Give the extent of all Plasmodium falciparum-infected red blood cells.
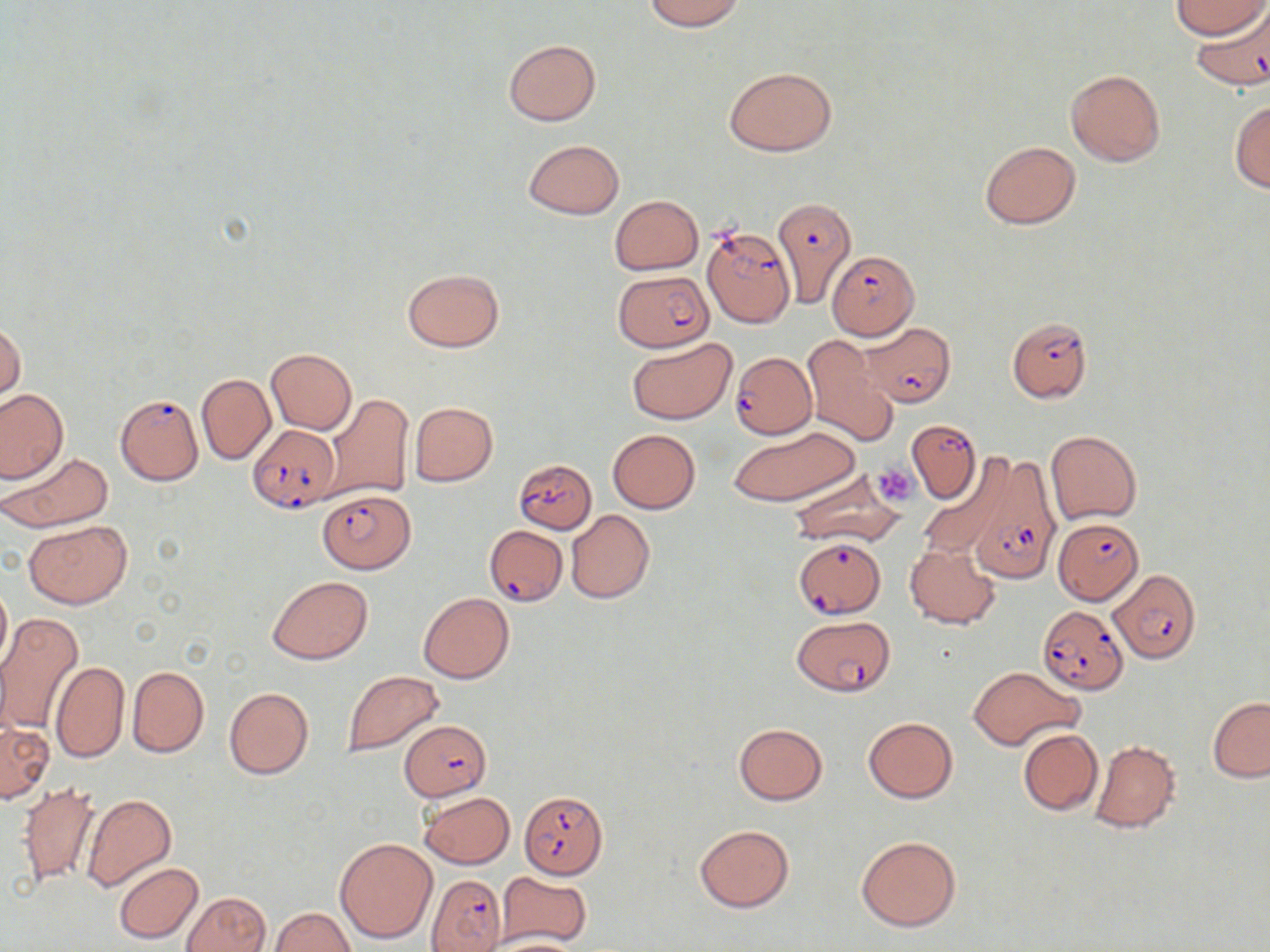

Approximate bounding boxes as (x1,y1)-(x2,y2) corner pairs in pixels.
Plasmodium falciparum-infected red blood cells (subset): (1190,2)-(1270,90), (771,197)-(856,308), (703,227)-(793,327), (829,251)-(920,339), (614,271)-(712,350), (1006,316)-(1093,402), (860,323)-(956,407), (729,353)-(813,442), (115,393)-(204,486), (907,420)-(980,503), (249,422)-(340,512), (515,458)-(597,534), (964,458)-(1063,581), (317,488)-(416,573), (1053,518)-(1142,604), (486,523)-(568,605), (1108,569)-(1200,663), (1037,605)-(1128,694), (793,615)-(894,696), (400,719)-(492,800), (426,872)-(507,951).

Uninfected red blood cell locations (subset): (643,0)-(745,31), (1174,0)-(1265,38), (503,38)-(601,126), (725,66)-(837,156), (1066,69)-(1166,167), (1229,100)-(1270,193), (523,139)-(624,219), (978,140)-(1080,230), (610,196)-(703,274), (402,268)-(504,352), (1,320)-(25,402), (801,336)-(898,449), (628,338)-(736,423), (266,349)-(356,434), (196,372)-(274,465), (0,388)-(68,482), (326,394)-(414,502), (409,402)-(497,486), (729,425)-(860,507), (607,429)-(701,513), (1045,430)-(1142,524), (2,450)-(113,532), (917,465)-(1011,562), (786,469)-(906,546), (566,510)-(654,603), (25,520)-(130,609), (906,542)-(1000,629), (267,575)-(373,664), (0,578)-(11,675), (419,592)-(514,684), (0,612)-(84,736), (50,660)-(130,764), (127,666)-(209,757), (969,666)-(1081,751), (341,670)-(444,757), (224,687)-(313,778), (1208,696)-(1270,782), (863,717)-(957,802), (1,722)-(53,802), (733,723)-(828,804), (1018,729)-(1102,816), (1089,739)-(1180,834), (17,780)-(102,890), (419,791)-(516,869), (81,794)-(176,892), (694,823)-(795,913), (856,835)-(962,931), (335,838)-(438,945), (114,861)-(204,944), (497,872)-(591,946), (182,891)-(271,952), (270,907)-(356,951), (489,935)-(583,952). Platelet locations: (871,462)-(920,504). Slide-level diagnosis: Plasmodium falciparum. May-Grünwald-Giemsa stain. Thin blood smear. One field of a larger specimen. Image is 1270×952 pixels. 1000x magnification. Light microscopy.